Name the blood parasite species.
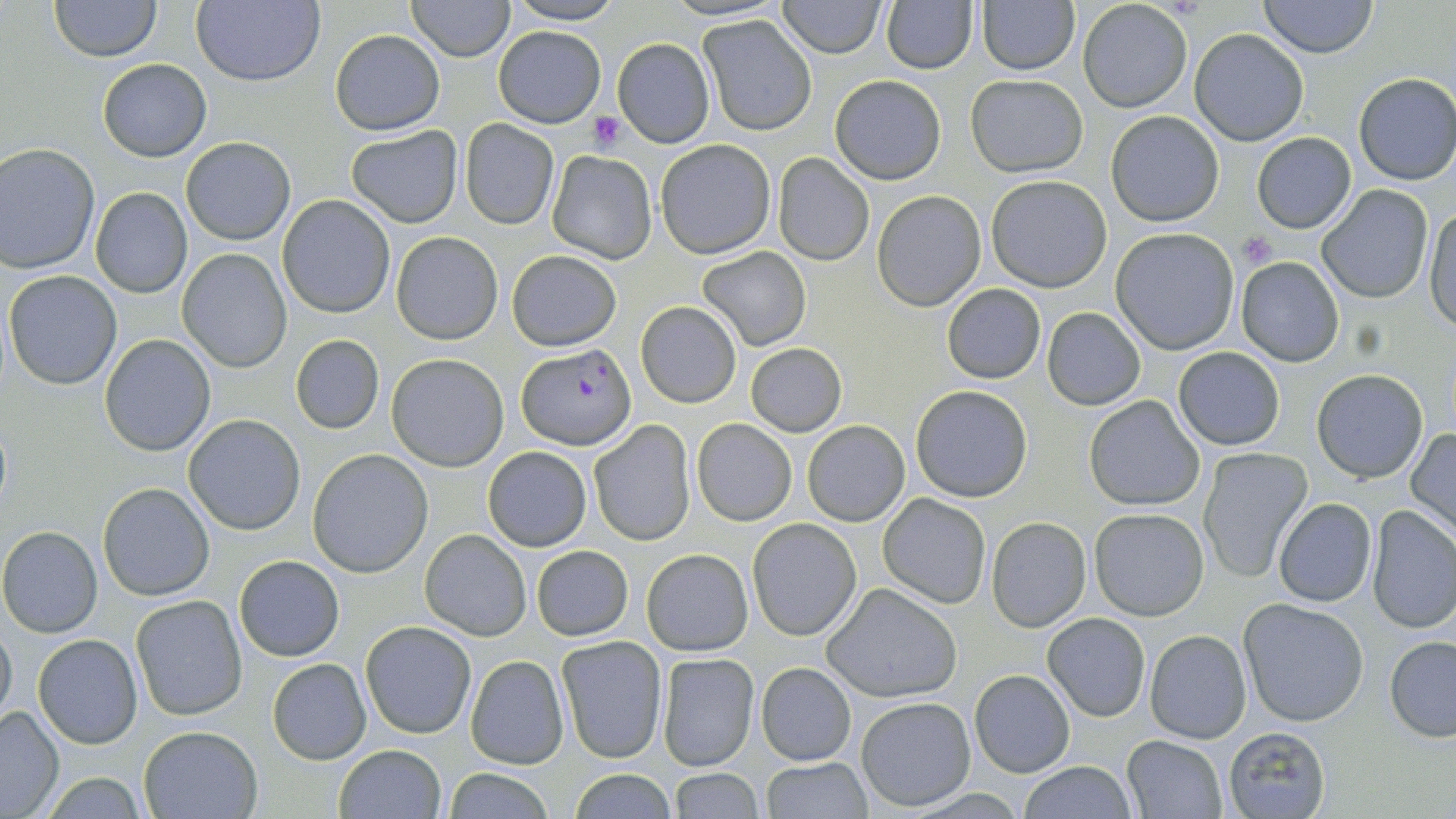

Plasmodium falciparum.

preparation = thin blood film
Plasmodium falciparum-infected red blood cell locations = approximate bounding boxes as (x1, y1, x2, y2) in pixels: (517, 342, 636, 450)
modality = optical microscopy
magnification = 1000x
uninfected red blood cell locations = approximate bounding boxes as (x1, y1, x2, y2) in pixels: (48, 0, 162, 61), (193, 0, 325, 88), (406, 0, 515, 60), (881, 0, 977, 74), (1258, 0, 1379, 58), (503, 1, 624, 25), (777, 1, 886, 56), (1076, 1, 1193, 114), (976, 2, 1079, 75), (697, 15, 817, 135), (496, 26, 606, 127), (1190, 29, 1308, 146), (330, 30, 444, 134), (612, 37, 714, 148), (98, 59, 211, 161), (1353, 72, 1456, 187), (965, 73, 1089, 178), (830, 74, 945, 184), (1105, 110, 1225, 227), (460, 120, 559, 230), (347, 125, 463, 228), (1252, 132, 1356, 233), (180, 137, 295, 244), (655, 140, 778, 259), (0, 144, 99, 273), (547, 149, 658, 265), (772, 152, 875, 267), (986, 174, 1113, 293), (1317, 186, 1434, 301), (90, 187, 192, 298), (873, 191, 988, 311), (277, 195, 396, 319), (1425, 205, 1456, 332), (1111, 227, 1240, 354), (391, 231, 502, 344), (696, 247, 812, 350), (177, 248, 292, 373), (506, 250, 621, 350), (1235, 256, 1345, 367), (4, 271, 122, 390), (941, 285, 1046, 383), (636, 302, 742, 408), (1042, 307, 1146, 410), (290, 334, 385, 435), (98, 335, 215, 456), (746, 343, 846, 437), (1173, 347, 1285, 450), (385, 353, 509, 471), (1312, 369, 1428, 482), (910, 385, 1034, 502), (1083, 395, 1206, 511), (183, 414, 306, 535), (691, 419, 798, 526), (589, 420, 696, 546), (802, 420, 911, 527), (1405, 429, 1456, 536), (1197, 446, 1311, 580), (482, 447, 592, 551), (308, 449, 433, 577), (97, 483, 214, 601), (878, 494, 991, 608), (1273, 499, 1377, 606), (1367, 505, 1456, 634), (1088, 508, 1211, 622), (986, 517, 1091, 632), (747, 518, 861, 641), (0, 527, 102, 637), (420, 529, 532, 641), (531, 545, 633, 640), (641, 547, 754, 657), (234, 554, 344, 661), (824, 584, 962, 704), (130, 594, 248, 720), (1236, 598, 1370, 727), (1043, 612, 1151, 722), (361, 621, 477, 739), (0, 622, 16, 730), (1144, 629, 1253, 744), (33, 635, 143, 749), (556, 635, 667, 763), (1384, 637, 1456, 741), (657, 652, 759, 772), (464, 654, 570, 769), (267, 658, 371, 764), (755, 662, 857, 765), (969, 669, 1076, 778), (855, 696, 976, 811), (0, 704, 64, 817), (1221, 726, 1331, 819), (138, 727, 262, 818), (1120, 735, 1228, 819), (333, 745, 447, 818), (759, 757, 872, 818), (1017, 760, 1136, 819), (439, 767, 558, 819), (667, 767, 765, 819), (567, 768, 678, 819), (32, 772, 157, 817)
field of view = single
platelet locations = approximate bounding boxes as (x1, y1, x2, y2) in pixels: (587, 111, 623, 153), (1239, 231, 1279, 268)
image size = 1456×819 pixels
stain = May-Grünwald-Giemsa